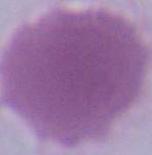
Micrograph. An erythrocyte is shown. 1000x magnification.